Name the blood parasite species.
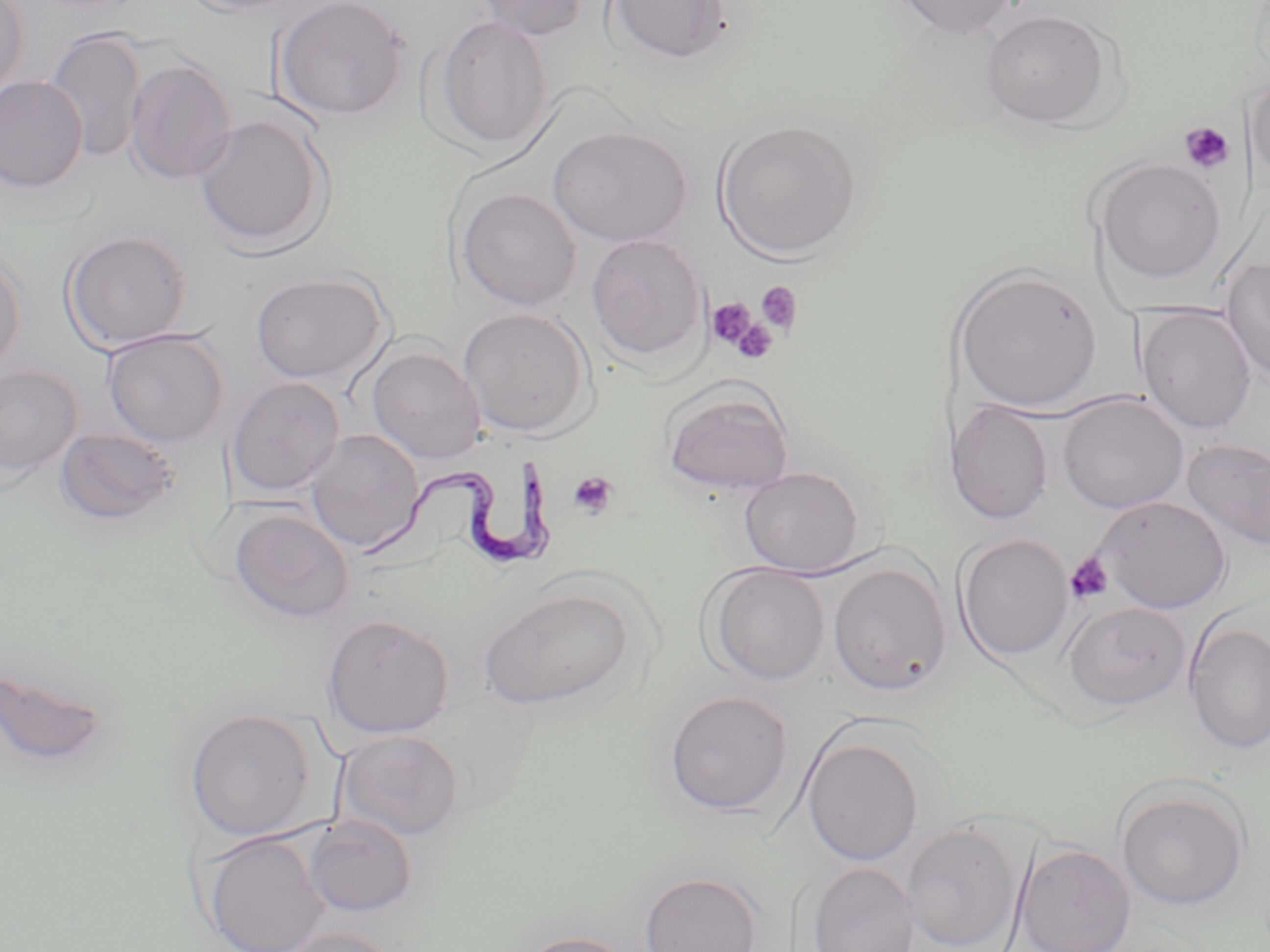

Trypanosoma brucei.

Summary:
  - Coordinate format: approximate bounding boxes as (x1, y1, x2, y2) in pixels
  - Trypanosoma brucei locations: (355, 456, 557, 571)
  - Uninfected red blood cell locations: (0, 0, 30, 105), (179, 0, 306, 16), (470, 0, 593, 41), (603, 0, 736, 67), (887, 0, 1020, 39), (273, 1, 412, 122), (979, 8, 1118, 130), (433, 13, 554, 154), (46, 26, 148, 165), (124, 57, 237, 186), (1245, 73, 1269, 192), (0, 76, 89, 193), (193, 112, 333, 255), (714, 119, 863, 259), (549, 125, 692, 246), (1091, 156, 1227, 285), (456, 186, 582, 312), (62, 230, 193, 352), (586, 233, 709, 363), (0, 250, 27, 379), (1220, 255, 1270, 387), (951, 264, 1103, 413), (249, 270, 391, 385), (1136, 305, 1257, 435), (458, 306, 595, 438), (102, 329, 229, 448), (366, 345, 487, 464), (0, 364, 82, 483), (227, 376, 345, 497), (658, 381, 797, 498), (1056, 393, 1189, 514), (945, 401, 1054, 525), (54, 425, 185, 527), (305, 429, 424, 552), (1182, 438, 1270, 551), (739, 466, 867, 575), (1093, 495, 1231, 613), (230, 508, 355, 623), (955, 533, 1074, 663), (827, 560, 952, 696), (703, 563, 831, 685), (479, 586, 635, 709), (1061, 600, 1191, 712), (321, 614, 455, 739), (1184, 620, 1270, 754), (0, 663, 114, 772), (663, 689, 796, 817), (185, 707, 317, 841), (336, 729, 465, 841), (802, 732, 925, 867), (1114, 782, 1251, 911), (302, 814, 418, 918), (903, 819, 1025, 952), (199, 831, 332, 952), (1014, 843, 1137, 952), (806, 861, 918, 952), (638, 870, 764, 952), (274, 926, 406, 952), (513, 930, 642, 952)
  - Platelet locations: (1179, 121, 1236, 174), (755, 281, 804, 335), (706, 297, 759, 351), (729, 318, 778, 364), (567, 470, 620, 520), (1065, 552, 1114, 604)
  - Magnification: 1000x
  - Modality: optical microscopy
  - Preparation: thin blood film
  - Image size: 1270×952 pixels
  - Stain: May-Grünwald-Giemsa
  - Field of view: one of a larger specimen